State which parasite is depicted.
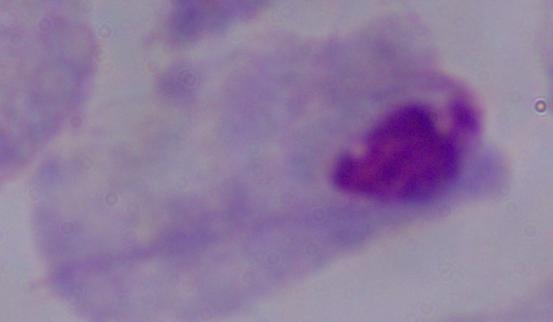

This is a trichomonad.

{
  "modality": "photomicrograph",
  "magnification": "1000x"
}